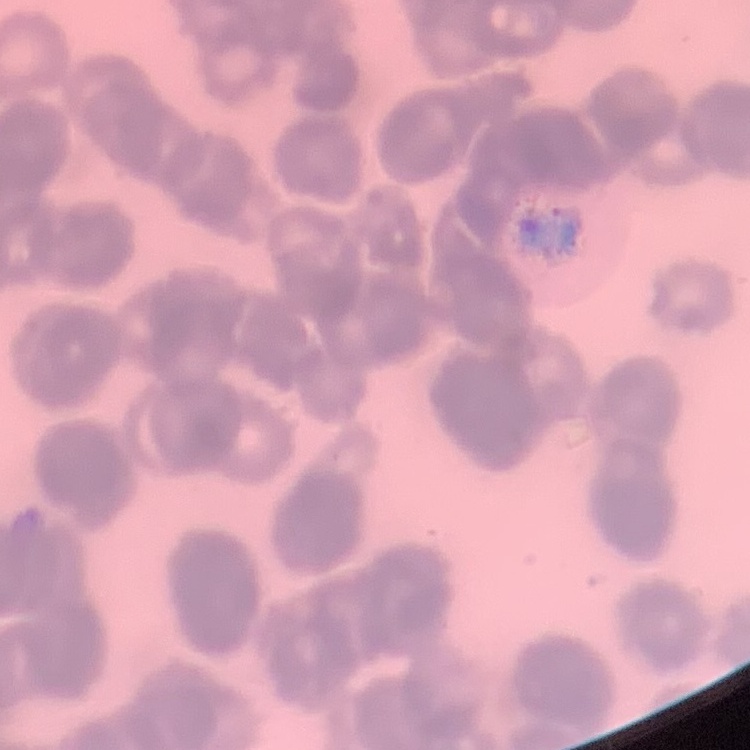
red blood cell morphology = rouleaux formation
image type = one tile cut from a larger photomicrograph
stain = Field's or Giemsa
preparation = thin blood smear